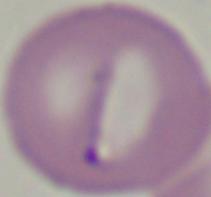
Summary:
  - Identification: Babesia
  - Magnification: 1000x
  - Modality: photomicrograph